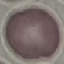

Summary:
  - Malaria status: uninfected
  - Preparation: thin blood film
  - Image type: cell patch, automatically extracted from a larger field of view and resized to 64 × 64 pixels
  - Capture: smartphone camera at the microscope eyepiece
  - Stain: Giemsa